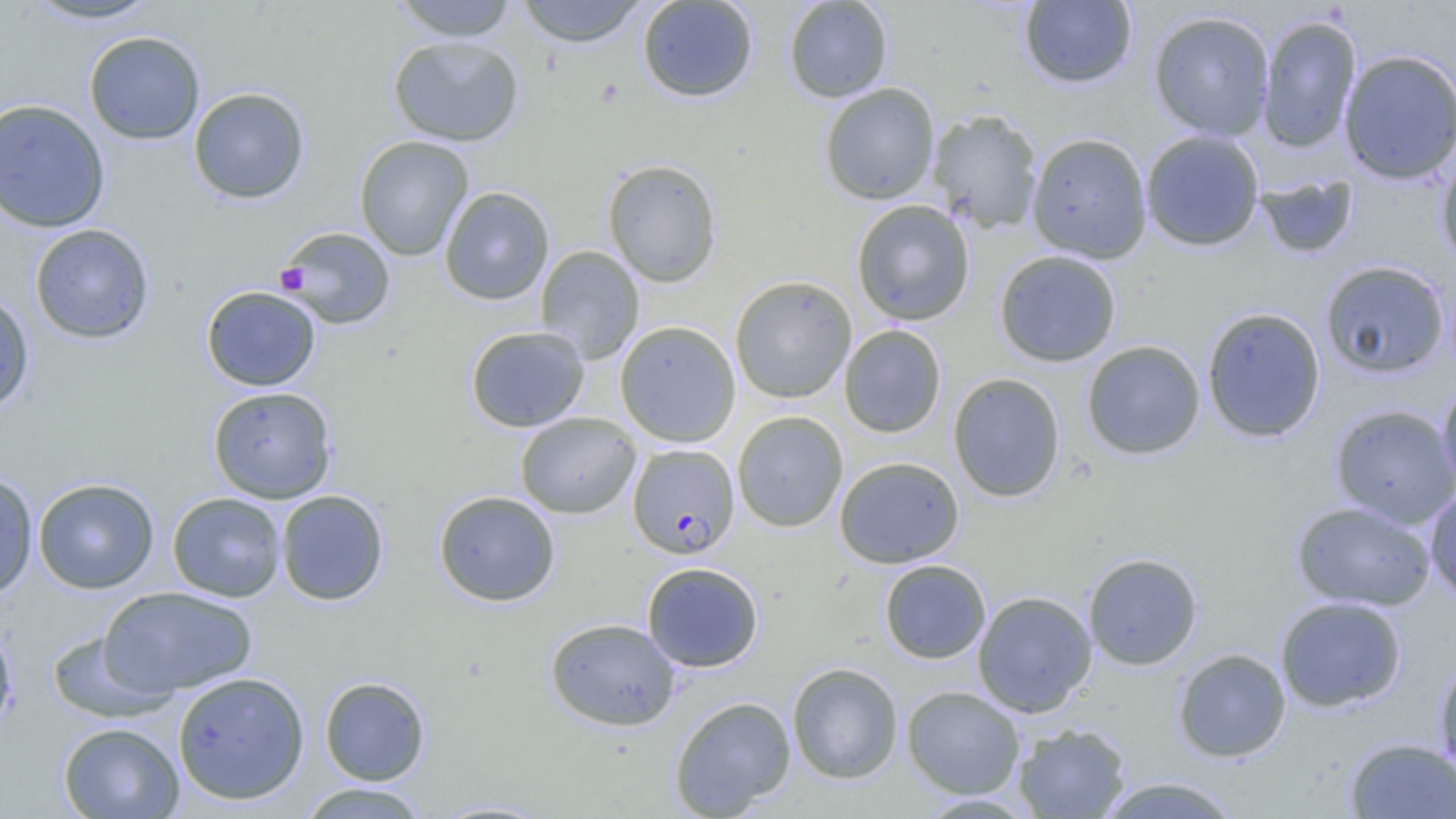

Approximate bounding boxes as named x1/y1/x2/y2 corners in pixels. Uninfected red blood cell locations: (x1=21, y1=0, x2=165, y2=26), (x1=390, y1=0, x2=520, y2=42), (x1=516, y1=0, x2=649, y2=47), (x1=637, y1=0, x2=758, y2=103), (x1=784, y1=0, x2=894, y2=103), (x1=1019, y1=1, x2=1138, y2=89), (x1=1148, y1=10, x2=1275, y2=141), (x1=1256, y1=14, x2=1363, y2=154), (x1=83, y1=30, x2=205, y2=145), (x1=387, y1=35, x2=524, y2=147), (x1=1338, y1=48, x2=1456, y2=185), (x1=819, y1=83, x2=940, y2=205), (x1=188, y1=86, x2=310, y2=204), (x1=0, y1=98, x2=110, y2=233), (x1=928, y1=109, x2=1044, y2=233), (x1=1140, y1=130, x2=1264, y2=251), (x1=1026, y1=132, x2=1153, y2=263), (x1=354, y1=135, x2=473, y2=261), (x1=1436, y1=150, x2=1456, y2=271), (x1=601, y1=158, x2=723, y2=287), (x1=1256, y1=173, x2=1359, y2=259), (x1=439, y1=186, x2=555, y2=306), (x1=851, y1=200, x2=975, y2=326), (x1=29, y1=223, x2=155, y2=344), (x1=277, y1=226, x2=396, y2=330), (x1=535, y1=245, x2=645, y2=364), (x1=994, y1=250, x2=1122, y2=367), (x1=1319, y1=260, x2=1451, y2=379), (x1=730, y1=275, x2=857, y2=403), (x1=200, y1=285, x2=321, y2=391), (x1=0, y1=289, x2=35, y2=415), (x1=1201, y1=306, x2=1326, y2=442), (x1=615, y1=320, x2=741, y2=448), (x1=465, y1=325, x2=589, y2=432), (x1=839, y1=325, x2=947, y2=438), (x1=1083, y1=331, x2=1326, y2=450), (x1=1081, y1=340, x2=1206, y2=460), (x1=948, y1=373, x2=1066, y2=503), (x1=1437, y1=377, x2=1456, y2=493), (x1=207, y1=386, x2=337, y2=503), (x1=1330, y1=403, x2=1456, y2=528), (x1=732, y1=411, x2=849, y2=532), (x1=515, y1=412, x2=641, y2=519), (x1=834, y1=456, x2=965, y2=568), (x1=0, y1=471, x2=38, y2=600), (x1=32, y1=477, x2=160, y2=594), (x1=1424, y1=488, x2=1456, y2=604), (x1=276, y1=489, x2=389, y2=606), (x1=433, y1=490, x2=561, y2=607), (x1=167, y1=492, x2=286, y2=602), (x1=1291, y1=501, x2=1435, y2=611), (x1=1082, y1=552, x2=1203, y2=670), (x1=879, y1=560, x2=991, y2=664), (x1=641, y1=562, x2=765, y2=672), (x1=99, y1=586, x2=259, y2=697), (x1=973, y1=590, x2=1097, y2=717), (x1=1275, y1=596, x2=1407, y2=713), (x1=544, y1=617, x2=681, y2=731), (x1=0, y1=620, x2=19, y2=740), (x1=44, y1=630, x2=172, y2=723), (x1=1173, y1=649, x2=1291, y2=763), (x1=1433, y1=654, x2=1456, y2=778), (x1=787, y1=662, x2=904, y2=784), (x1=172, y1=671, x2=310, y2=805), (x1=319, y1=676, x2=431, y2=785), (x1=901, y1=685, x2=1026, y2=799), (x1=669, y1=695, x2=796, y2=817), (x1=58, y1=722, x2=185, y2=818), (x1=1013, y1=722, x2=1131, y2=818), (x1=1345, y1=738, x2=1456, y2=818), (x1=1095, y1=776, x2=1243, y2=818), (x1=296, y1=782, x2=431, y2=819), (x1=425, y1=799, x2=558, y2=818). Plasmodium falciparum-infected red blood cell locations: (x1=627, y1=443, x2=740, y2=559). Platelet locations: (x1=275, y1=262, x2=309, y2=295). Slide-level diagnosis: Plasmodium falciparum. Light microscopy. Thin blood film. Image is 1456×819 pixels. 1000x magnification. One field of a larger specimen.